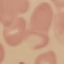

Malaria status: uninfected. Cell patch, automatically extracted from a larger field of view and resized to 64 × 64 pixels. Acquired by smartphone through the microscope eyepiece. Thin blood smear. Giemsa stain.